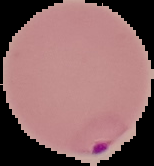
image size = 154×166 pixels
malaria status = parasitized
preparation = thin blood smear
image type = cell region segmented out of the field of view; surrounding area masked to black